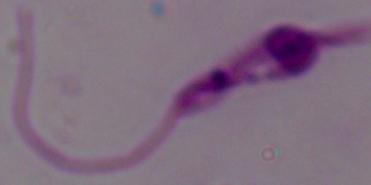

Summary:
  - Identification: Leishmania
  - Magnification: 1000x
  - Modality: photomicrograph